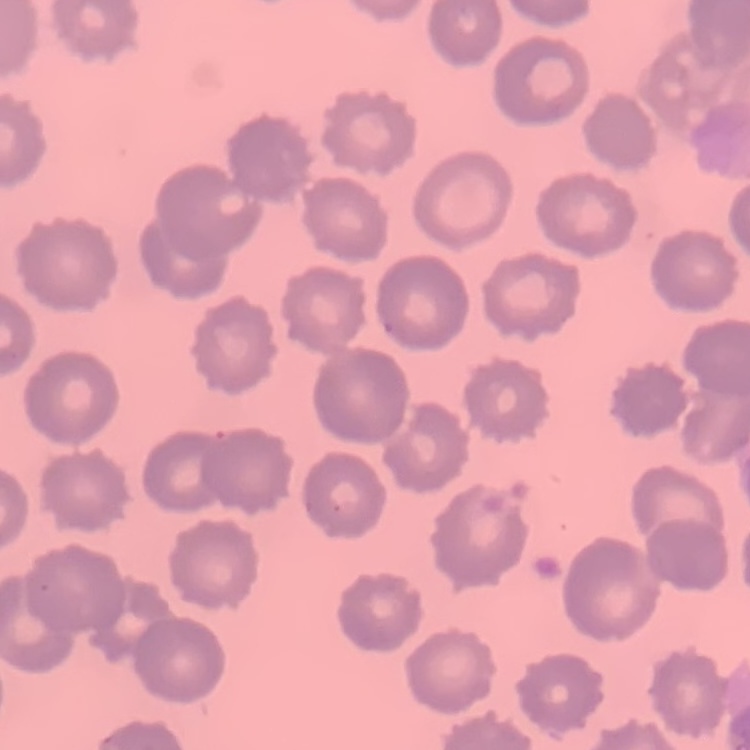

Summary:
  - Erythrocyte morphology: no rouleaux formation
  - Preparation: thin blood film
  - Image type: one tile cut from a larger photomicrograph
  - Stain: Field's or Giemsa